Which red blood cells are P. falciparum-infected, and which are of indeterminate infection status?
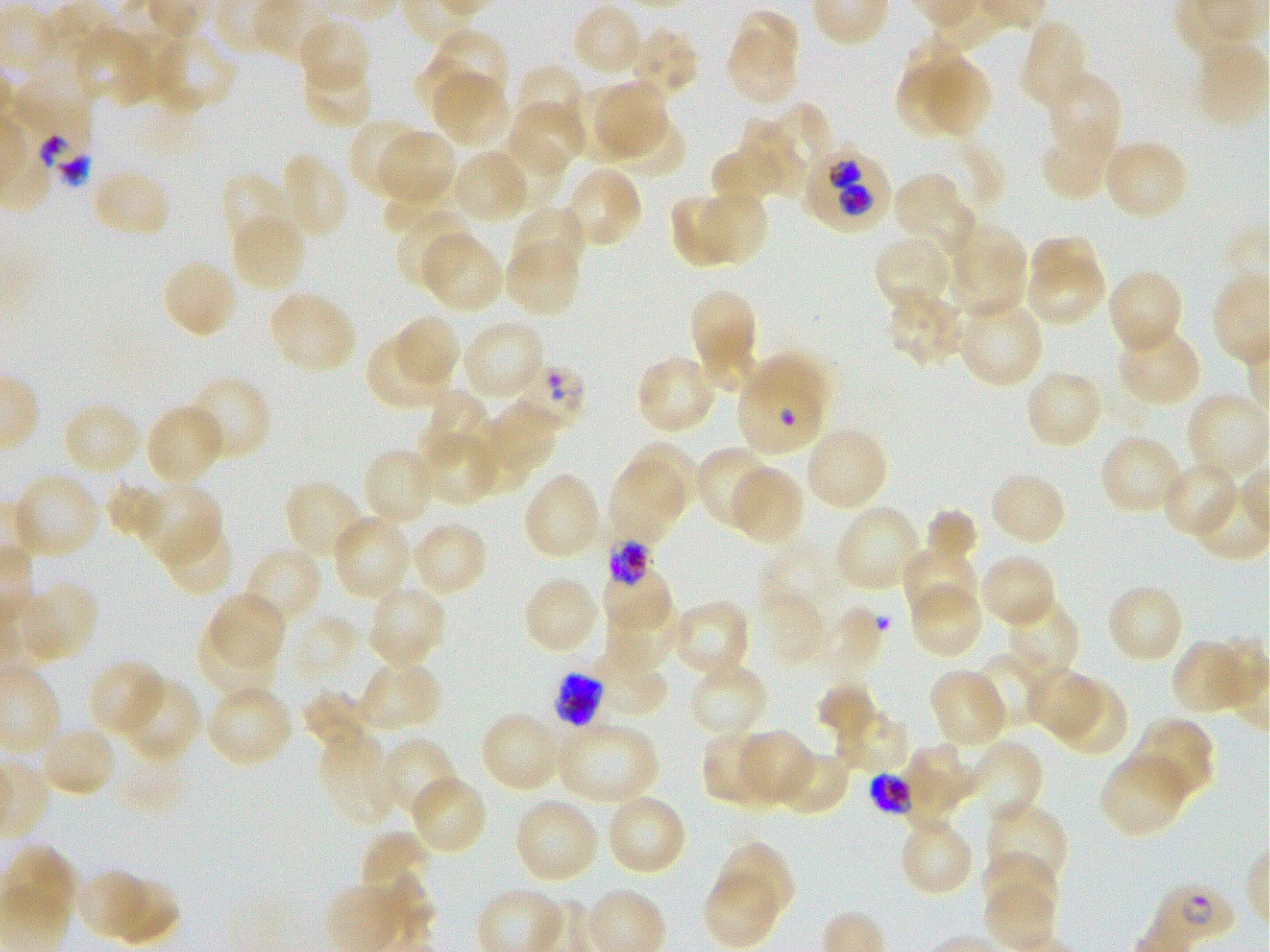

Approximate bounding rectangles given as corner coordinates in pixels from the top-left. Not every red blood cell is marked. A life-cycle stage — or a range of stages, where the recorded stages span more than one — follows each staged infected red blood cell.
Infected red blood cells: (x1=801, y1=144, x2=890, y2=231); (x1=737, y1=354, x2=830, y2=459); (x1=605, y1=538, x2=658, y2=586) late trophozoite to late schizont; (x1=550, y1=671, x2=605, y2=727) schizont; (x1=865, y1=770, x2=911, y2=820) schizont; (x1=1143, y1=878, x2=1239, y2=952) ring.
Red blood cells of indeterminate infection status: (x1=12, y1=83, x2=96, y2=190), (x1=514, y1=361, x2=586, y2=430).

Summary:
  - Locations of uninfected red blood cells: (x1=571, y1=3, x2=645, y2=80), (x1=724, y1=11, x2=802, y2=108), (x1=296, y1=19, x2=371, y2=94), (x1=1019, y1=19, x2=1092, y2=111), (x1=627, y1=25, x2=699, y2=101), (x1=77, y1=27, x2=150, y2=109), (x1=435, y1=29, x2=509, y2=98), (x1=133, y1=30, x2=236, y2=116), (x1=411, y1=55, x2=500, y2=120), (x1=301, y1=58, x2=374, y2=130), (x1=928, y1=61, x2=992, y2=142), (x1=513, y1=62, x2=587, y2=137), (x1=892, y1=66, x2=954, y2=137), (x1=1046, y1=71, x2=1122, y2=162), (x1=435, y1=74, x2=511, y2=144), (x1=596, y1=81, x2=667, y2=162), (x1=564, y1=85, x2=633, y2=158), (x1=507, y1=100, x2=587, y2=175), (x1=776, y1=101, x2=831, y2=166), (x1=602, y1=111, x2=686, y2=181), (x1=348, y1=118, x2=423, y2=197), (x1=737, y1=118, x2=810, y2=200), (x1=1041, y1=125, x2=1119, y2=202), (x1=381, y1=131, x2=452, y2=200), (x1=493, y1=136, x2=568, y2=210), (x1=1102, y1=138, x2=1189, y2=222), (x1=450, y1=148, x2=531, y2=224), (x1=276, y1=152, x2=349, y2=240), (x1=713, y1=153, x2=782, y2=204), (x1=562, y1=165, x2=643, y2=250), (x1=383, y1=166, x2=456, y2=228), (x1=91, y1=167, x2=172, y2=239), (x1=221, y1=172, x2=295, y2=254), (x1=892, y1=172, x2=973, y2=260), (x1=698, y1=189, x2=768, y2=265), (x1=670, y1=195, x2=734, y2=267), (x1=512, y1=205, x2=589, y2=277), (x1=395, y1=209, x2=474, y2=291), (x1=230, y1=211, x2=308, y2=295), (x1=947, y1=221, x2=1029, y2=319), (x1=419, y1=232, x2=504, y2=313), (x1=873, y1=233, x2=954, y2=315), (x1=504, y1=235, x2=582, y2=318), (x1=1033, y1=236, x2=1097, y2=287), (x1=161, y1=258, x2=238, y2=339), (x1=1031, y1=260, x2=1106, y2=329), (x1=1107, y1=267, x2=1184, y2=355), (x1=886, y1=286, x2=968, y2=365), (x1=267, y1=288, x2=357, y2=375), (x1=690, y1=290, x2=754, y2=357), (x1=955, y1=297, x2=1045, y2=389), (x1=395, y1=316, x2=461, y2=384), (x1=460, y1=319, x2=546, y2=405), (x1=1115, y1=323, x2=1202, y2=406), (x1=369, y1=333, x2=448, y2=406), (x1=703, y1=343, x2=758, y2=391), (x1=636, y1=355, x2=717, y2=434), (x1=1024, y1=369, x2=1104, y2=451), (x1=186, y1=374, x2=271, y2=463), (x1=430, y1=390, x2=486, y2=467), (x1=1185, y1=393, x2=1270, y2=483), (x1=488, y1=400, x2=558, y2=471), (x1=61, y1=401, x2=143, y2=477), (x1=144, y1=403, x2=225, y2=488), (x1=473, y1=419, x2=534, y2=490), (x1=803, y1=426, x2=889, y2=512), (x1=419, y1=428, x2=495, y2=505), (x1=1098, y1=433, x2=1186, y2=516), (x1=633, y1=441, x2=698, y2=514), (x1=362, y1=447, x2=440, y2=528), (x1=695, y1=447, x2=776, y2=531), (x1=1161, y1=461, x2=1241, y2=540), (x1=609, y1=462, x2=684, y2=546), (x1=730, y1=465, x2=805, y2=547), (x1=522, y1=470, x2=603, y2=562), (x1=988, y1=470, x2=1067, y2=548), (x1=16, y1=475, x2=96, y2=553), (x1=102, y1=478, x2=167, y2=538), (x1=283, y1=478, x2=369, y2=562), (x1=1190, y1=481, x2=1270, y2=561), (x1=139, y1=488, x2=221, y2=564), (x1=833, y1=503, x2=925, y2=593), (x1=924, y1=508, x2=978, y2=575), (x1=332, y1=515, x2=413, y2=602), (x1=158, y1=519, x2=235, y2=597), (x1=409, y1=521, x2=489, y2=597), (x1=902, y1=543, x2=977, y2=621), (x1=243, y1=544, x2=323, y2=627), (x1=978, y1=553, x2=1058, y2=629), (x1=601, y1=566, x2=674, y2=632), (x1=522, y1=575, x2=601, y2=656), (x1=907, y1=580, x2=983, y2=659), (x1=24, y1=581, x2=97, y2=662), (x1=1105, y1=583, x2=1185, y2=665), (x1=365, y1=584, x2=447, y2=670), (x1=763, y1=591, x2=825, y2=661), (x1=210, y1=592, x2=287, y2=667), (x1=1003, y1=595, x2=1079, y2=681), (x1=669, y1=598, x2=750, y2=680), (x1=604, y1=599, x2=681, y2=673), (x1=196, y1=620, x2=275, y2=698), (x1=1171, y1=640, x2=1252, y2=715), (x1=976, y1=651, x2=1050, y2=729), (x1=574, y1=652, x2=666, y2=724), (x1=87, y1=659, x2=167, y2=740), (x1=355, y1=659, x2=442, y2=735), (x1=687, y1=659, x2=769, y2=739), (x1=929, y1=667, x2=1009, y2=751), (x1=1024, y1=667, x2=1102, y2=741), (x1=117, y1=676, x2=200, y2=763), (x1=1048, y1=677, x2=1129, y2=758), (x1=816, y1=683, x2=879, y2=734), (x1=208, y1=687, x2=292, y2=762), (x1=302, y1=691, x2=374, y2=749), (x1=836, y1=709, x2=908, y2=774), (x1=479, y1=711, x2=564, y2=794), (x1=1133, y1=717, x2=1215, y2=803), (x1=555, y1=721, x2=659, y2=806), (x1=317, y1=726, x2=399, y2=825), (x1=45, y1=728, x2=117, y2=792), (x1=738, y1=729, x2=815, y2=806), (x1=701, y1=730, x2=783, y2=807), (x1=377, y1=736, x2=459, y2=820), (x1=960, y1=741, x2=1044, y2=830), (x1=903, y1=743, x2=978, y2=834), (x1=771, y1=749, x2=852, y2=816), (x1=1098, y1=752, x2=1189, y2=839), (x1=414, y1=774, x2=488, y2=851), (x1=605, y1=792, x2=687, y2=877), (x1=513, y1=795, x2=602, y2=884), (x1=984, y1=801, x2=1066, y2=888), (x1=901, y1=824, x2=974, y2=898), (x1=359, y1=832, x2=428, y2=890), (x1=716, y1=842, x2=795, y2=922), (x1=982, y1=850, x2=1055, y2=921), (x1=77, y1=868, x2=172, y2=944), (x1=705, y1=871, x2=779, y2=947)
  - Life-cycle stages observed: ring, schizont
  - Stain: Giemsa
  - Field of view: single
  - Donor blood group: O+
  - Preparation: thin blood smear
  - Culture: in-vitro P. falciparum strain 3D7, static
  - Objective: 100x, oil immersion, numerical aperture 1.25
  - Image size: 1270×952 pixels